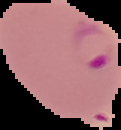

preparation = thin blood smear
malaria status = parasitized
image type = segmented cell region on a black background
image size = 121×130 pixels